Locate every Plasmodium parasite.
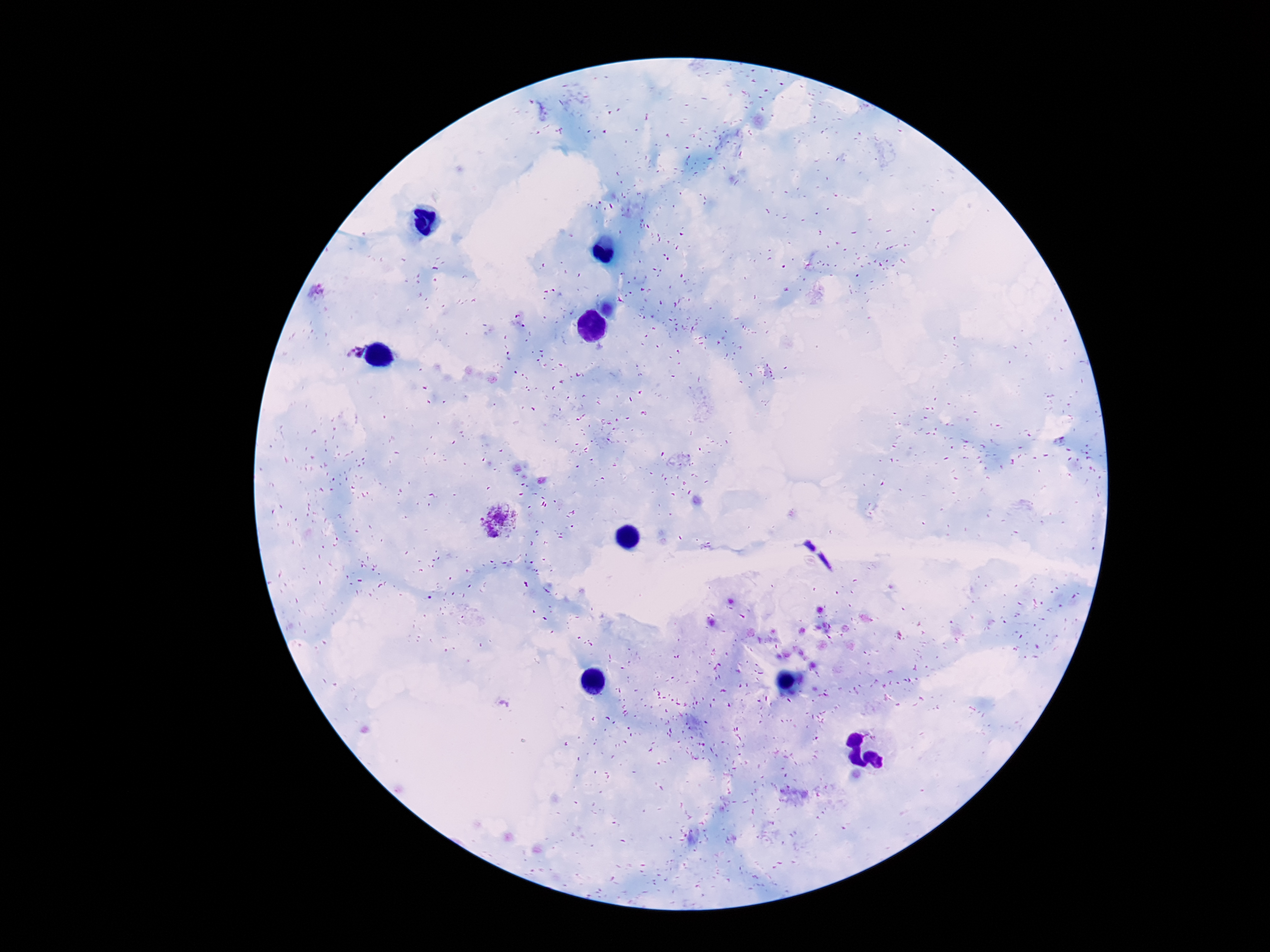

Approximate object centers, in pixels from the top-left corner.
Plasmodium parasites: (x=352, y=350), (x=501, y=521).

patient malaria status = positive
capture = smartphone camera through the microscope eyepiece
stain = Giemsa
field of view = single
magnification = 100x
preparation = thick blood smear
image size = 1270×952 pixels